Point out every malaria parasite and every leukocyte.
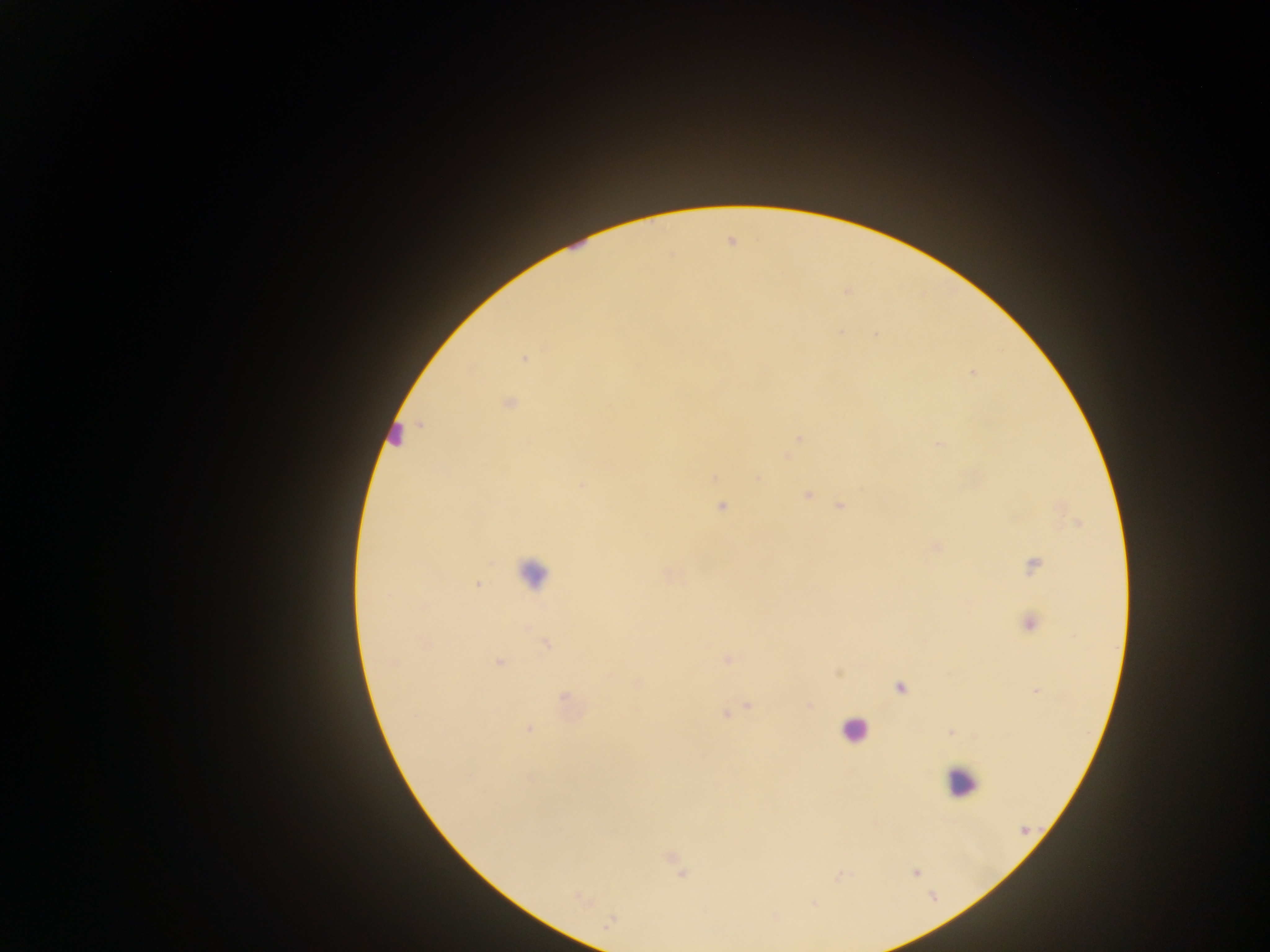

Approximate centers as [x, y] in pixels.
Malaria parasites: [524, 358], [971, 373], [508, 403], [938, 445], [715, 477], [582, 485], [808, 495], [839, 506], [721, 507], [937, 546], [1033, 565], [478, 584], [1030, 624], [546, 644], [727, 659], [499, 662], [390, 664], [838, 673], [638, 684], [899, 688], [1035, 691], [565, 697], [810, 705], [749, 706], [725, 714], [528, 730], [951, 731], [1025, 831], [915, 873].
Leukocytes: [576, 245], [396, 434], [533, 572], [853, 729], [961, 781].

Mobile-phone photograph taken through the microscope. One field of view. Sample from Ghana. Thick blood film. Image is 1270×952 pixels.